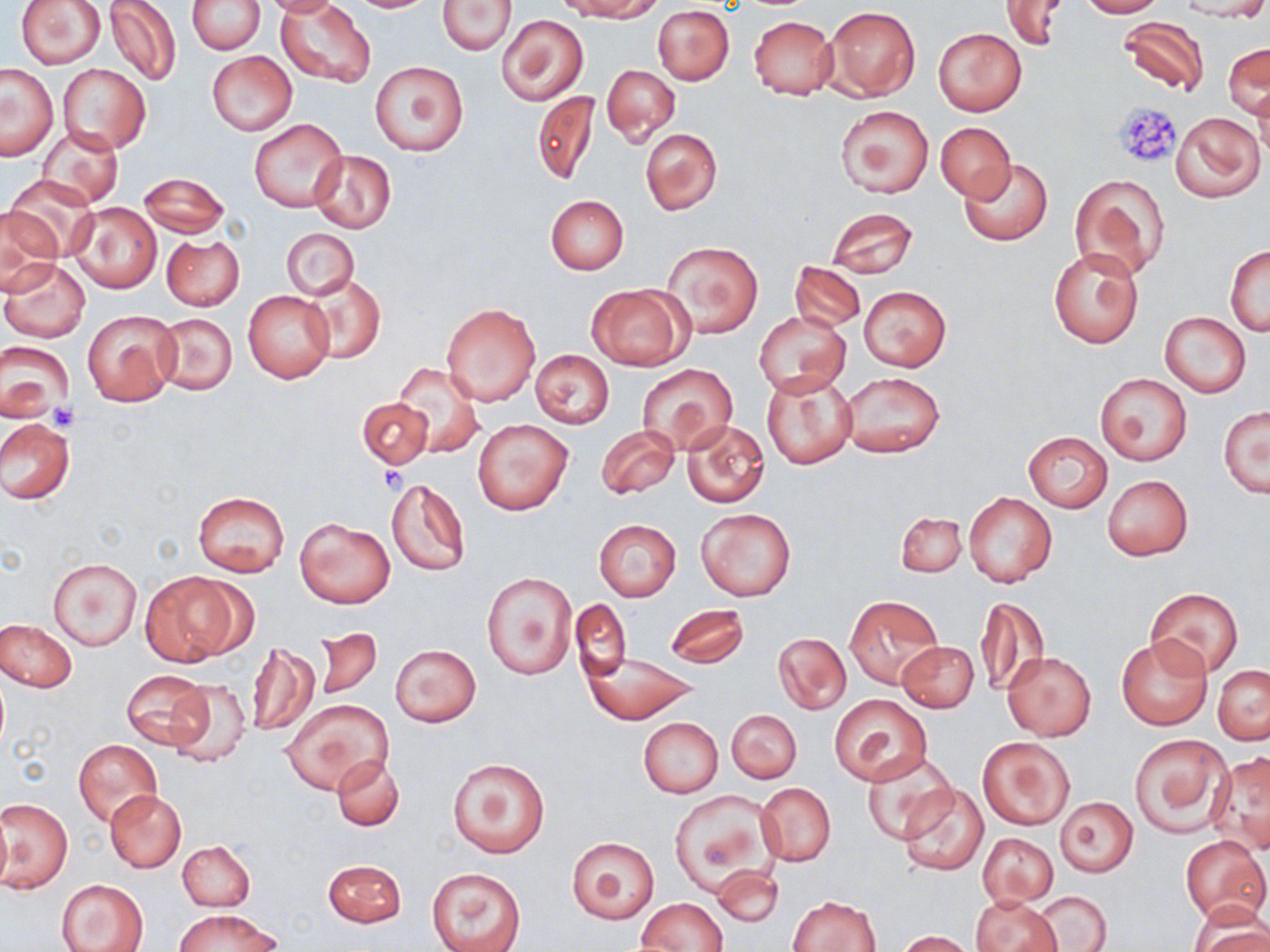
Approximate bounding boxes as (x1,y1)-(x2,y2) corner pairs in pixels. Platelet locations: (1112,101)-(1183,168), (48,403)-(78,431), (378,465)-(407,492). Uninfected red blood cell locations: (15,0)-(106,69), (105,0)-(182,87), (261,0)-(343,17), (345,0)-(437,13), (437,0)-(515,55), (567,0)-(661,21), (1001,0)-(1068,50), (1074,0)-(1163,17), (1173,0)-(1270,21), (187,1)-(264,55), (278,2)-(376,85), (654,5)-(735,85), (824,6)-(919,102), (499,15)-(587,105), (749,16)-(838,100), (1116,16)-(1211,98), (933,28)-(1027,116), (1224,43)-(1268,120), (207,51)-(297,136), (370,61)-(469,155), (57,64)-(151,153), (0,65)-(58,159), (601,65)-(680,145), (532,91)-(598,187), (834,105)-(933,198), (1172,113)-(1264,201), (249,117)-(347,213), (935,122)-(1015,200), (37,125)-(123,209), (640,128)-(723,215), (310,150)-(396,233), (958,157)-(1053,246), (139,172)-(229,238), (1069,173)-(1169,280), (6,175)-(98,259), (545,195)-(629,274), (68,202)-(161,294), (0,207)-(62,293), (826,207)-(917,278), (282,228)-(358,301), (162,235)-(245,311), (663,240)-(763,338), (1226,244)-(1269,335), (1049,247)-(1144,349), (2,259)-(90,344), (791,261)-(865,332), (305,274)-(386,362), (587,284)-(690,372), (860,286)-(951,371), (243,291)-(333,383), (440,301)-(541,406), (82,309)-(180,407), (154,312)-(237,395), (754,312)-(849,397), (1160,312)-(1250,397), (1,342)-(74,425), (530,349)-(614,427), (393,363)-(485,457), (637,364)-(738,454), (838,371)-(946,457), (761,372)-(856,470), (1094,372)-(1192,466), (357,397)-(433,469), (1218,406)-(1269,497), (472,417)-(573,515), (0,418)-(74,506), (682,420)-(769,508), (596,424)-(679,499), (1022,431)-(1112,512), (1102,475)-(1192,561), (386,480)-(470,576), (193,491)-(290,579), (964,492)-(1058,588), (696,508)-(796,600), (895,511)-(966,577), (294,517)-(395,608), (594,519)-(681,601), (49,558)-(142,651), (140,572)-(244,666), (482,572)-(576,680), (1146,588)-(1244,678), (845,594)-(943,690), (977,595)-(1050,697), (571,599)-(632,679), (663,604)-(749,668), (1,619)-(76,691), (313,628)-(382,701), (773,632)-(851,715), (1115,635)-(1212,730), (246,640)-(319,737), (898,641)-(979,712), (389,644)-(480,727), (583,651)-(698,723), (1004,653)-(1095,740), (1213,665)-(1270,744), (122,670)-(213,750), (165,679)-(252,768), (830,693)-(932,786), (283,698)-(393,795), (727,709)-(801,784), (638,718)-(722,797), (1130,733)-(1232,837), (978,737)-(1073,829), (73,739)-(161,825), (1209,750)-(1270,854), (862,752)-(958,844), (332,755)-(404,831), (446,757)-(549,858), (757,783)-(835,866), (896,784)-(989,876), (105,789)-(186,871), (669,790)-(779,898), (1055,797)-(1138,876), (1,799)-(71,893), (0,809)-(11,893), (978,833)-(1057,907), (566,835)-(659,923), (1181,835)-(1270,926), (179,840)-(255,911), (322,859)-(406,928), (712,865)-(785,929), (426,867)-(527,952), (57,878)-(148,952), (1033,891)-(1111,951), (789,895)-(881,951), (971,895)-(1062,952), (636,898)-(727,951), (1190,904)-(1270,952), (176,909)-(279,952), (895,931)-(973,951). Slide-level diagnosis: negative for blood parasites. May-Grünwald-Giemsa stain. Image is 1270×952 pixels. One field of a larger specimen. Light microscopy. Thin blood smear. 1000x magnification.